Locate every parasitized RBC.
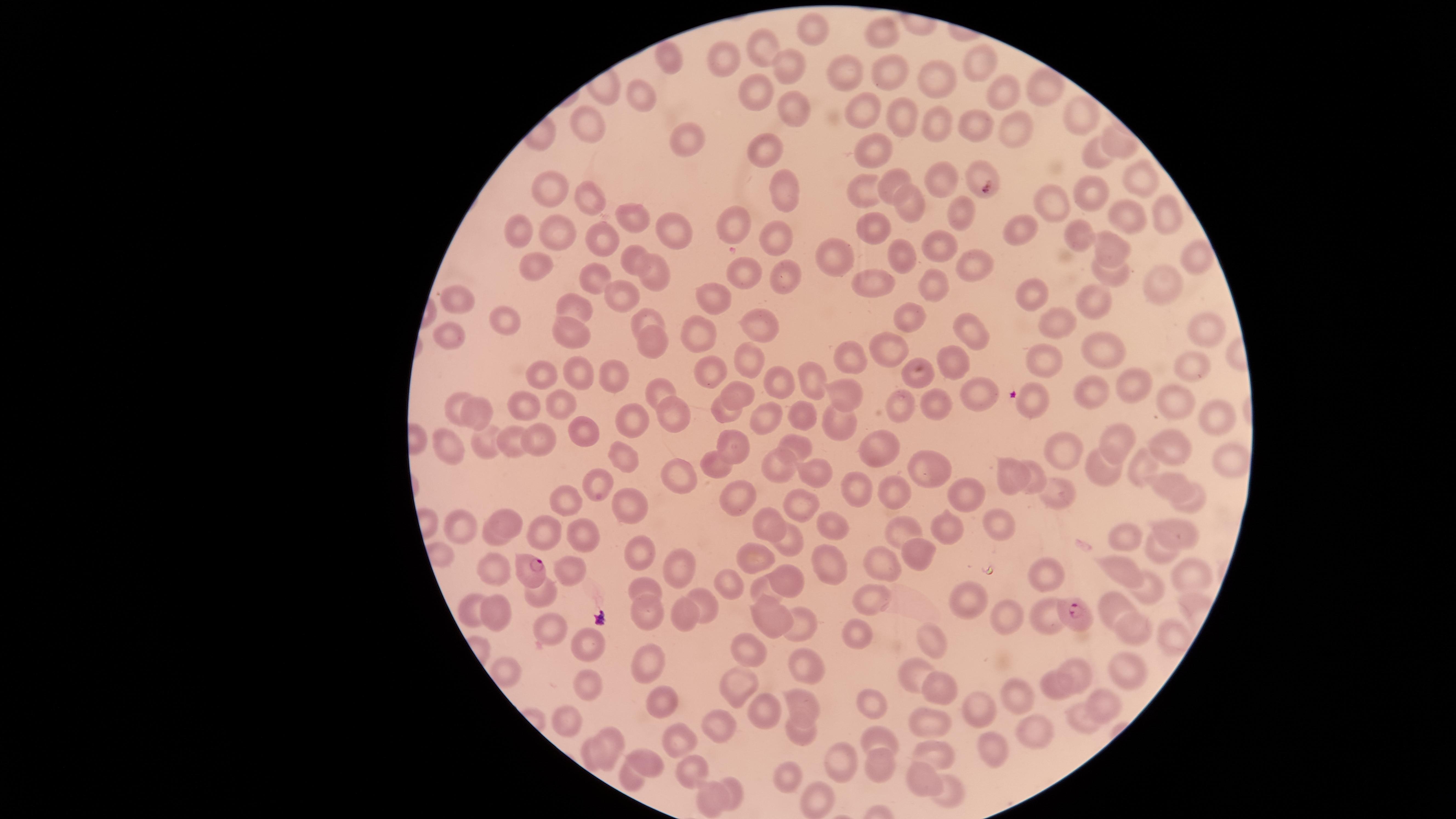

Approximate marker points as (x, y) in pixels.
Parasitized RBCs: (536, 572), (1071, 612).

image size = 1456×819 pixels
field of view = single
visible region = circular
uninfected RBCs = approximate marker points as (x, y) in pixels: (814, 30), (877, 31), (768, 46), (669, 61), (723, 61), (986, 61), (791, 65), (890, 69), (852, 73), (940, 81), (1040, 84), (755, 88), (998, 90), (641, 98), (796, 110), (856, 112), (1075, 112), (906, 115), (937, 120), (969, 124), (1014, 129), (592, 135), (688, 139), (771, 146), (872, 151), (1121, 151), (1091, 155), (980, 171), (940, 172), (1138, 177), (889, 181), (554, 190), (864, 190), (1097, 192), (784, 193), (586, 200), (912, 201), (1055, 202), (1162, 213), (962, 216), (634, 218), (1113, 222), (737, 226), (673, 228), (872, 230), (1018, 232), (521, 233), (1081, 235), (766, 236), (555, 238), (598, 238), (944, 248), (1111, 248), (634, 253), (908, 255), (965, 259), (836, 260), (1189, 262), (741, 266), (538, 267), (1111, 272), (591, 274), (655, 277), (789, 280), (934, 281), (1152, 286), (872, 288), (714, 294), (1030, 294), (460, 296), (629, 298), (1094, 301), (580, 305), (647, 318), (1044, 319), (765, 320), (505, 323), (909, 323), (572, 331), (1206, 331), (441, 334), (699, 338), (978, 338), (655, 340), (888, 347), (1097, 352), (745, 358), (848, 359), (1049, 359), (955, 363), (1186, 367), (708, 369), (611, 370), (583, 372), (544, 374), (916, 375), (809, 379), (1129, 379), (775, 382), (660, 390), (739, 392), (1082, 393), (982, 395), (841, 396), (1176, 401), (525, 403), (1034, 403), (566, 407), (899, 407), (933, 407), (801, 409), (727, 410), (452, 411), (671, 414), (765, 414), (1212, 414), (481, 416), (632, 417), (586, 430), (510, 434), (447, 437), (541, 442), (1178, 443), (737, 444), (1060, 444), (481, 445), (1123, 445), (885, 447), (803, 448), (625, 453), (1226, 460), (783, 461), (1148, 464), (719, 466), (1107, 470), (935, 471), (684, 475), (1013, 475), (1034, 475), (820, 478), (594, 480), (859, 480), (1168, 483), (1061, 488), (896, 491), (968, 498), (737, 500), (1192, 501), (629, 503), (564, 504), (799, 508), (510, 517), (825, 524), (896, 525), (944, 525), (1002, 525), (463, 526), (768, 526), (530, 528), (1182, 532), (588, 536), (785, 536), (1127, 536), (496, 541), (917, 546), (1153, 551), (824, 554), (766, 561), (889, 563), (637, 564), (679, 564), (1125, 567), (1190, 569), (782, 570), (502, 571), (573, 572), (1047, 576), (726, 580), (1153, 583), (768, 589), (641, 590), (547, 598), (873, 599), (974, 599), (1115, 603), (708, 604), (500, 608), (473, 610), (772, 610), (684, 615), (1001, 615), (641, 616), (1054, 618), (1131, 625), (799, 626), (554, 627), (855, 633), (1171, 637), (580, 641), (929, 641), (743, 646), (802, 660), (642, 663), (1078, 663), (1126, 667), (910, 670), (587, 680), (735, 680), (1065, 687), (938, 690), (804, 699), (1019, 699), (871, 703), (1108, 703), (985, 705), (666, 710), (764, 711), (568, 717), (1080, 717), (801, 729), (936, 729), (721, 733), (878, 736), (614, 738), (1039, 739), (667, 742), (992, 753), (930, 754), (599, 756), (836, 762), (651, 763), (878, 764), (689, 769), (795, 776), (638, 779), (924, 783), (734, 788), (811, 794), (949, 794), (703, 797)
preparation = thin smear of blood
stain = Giemsa
capture = smartphone photograph through the microscope eyepiece
species = Plasmodium falciparum